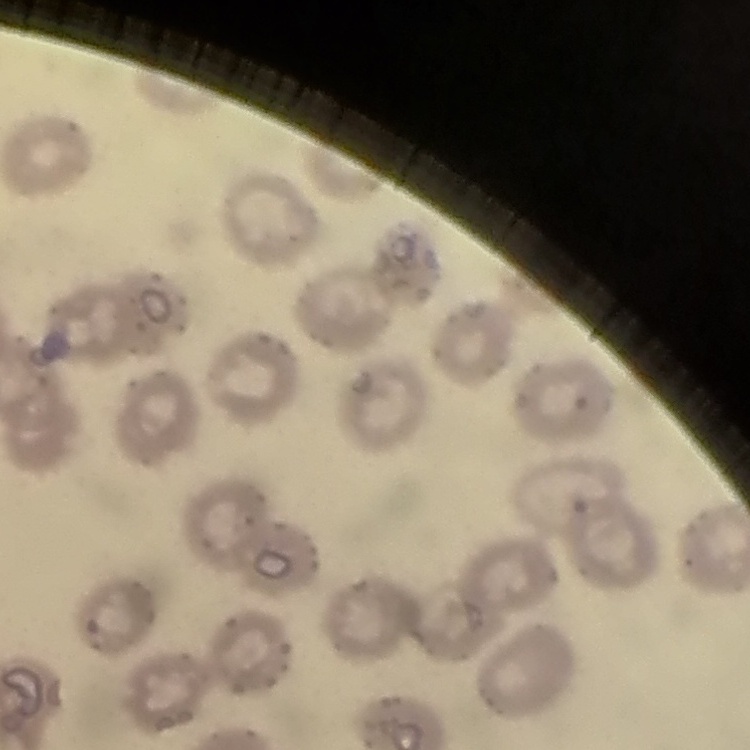

{
  "erythrocyte_morphology": "no rouleaux formation",
  "preparation": "thin blood smear",
  "stain": "Field's or Giemsa",
  "image_type": "one tile cut from a larger photomicrograph"
}